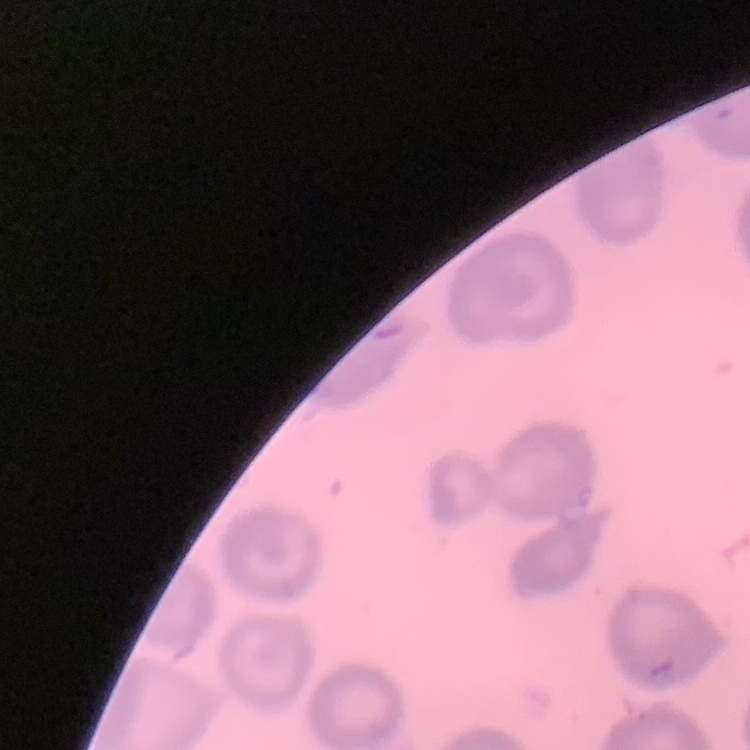
Summary:
  - Erythrocyte morphology: no rouleaux formation
  - Stain: Field's or Giemsa
  - Preparation: thin blood film
  - Image type: one tile cut from a larger photomicrograph